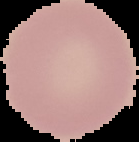
image size = 139×142 pixels
image type = segmented cell region on a black background
malaria status = uninfected
preparation = thin blood film